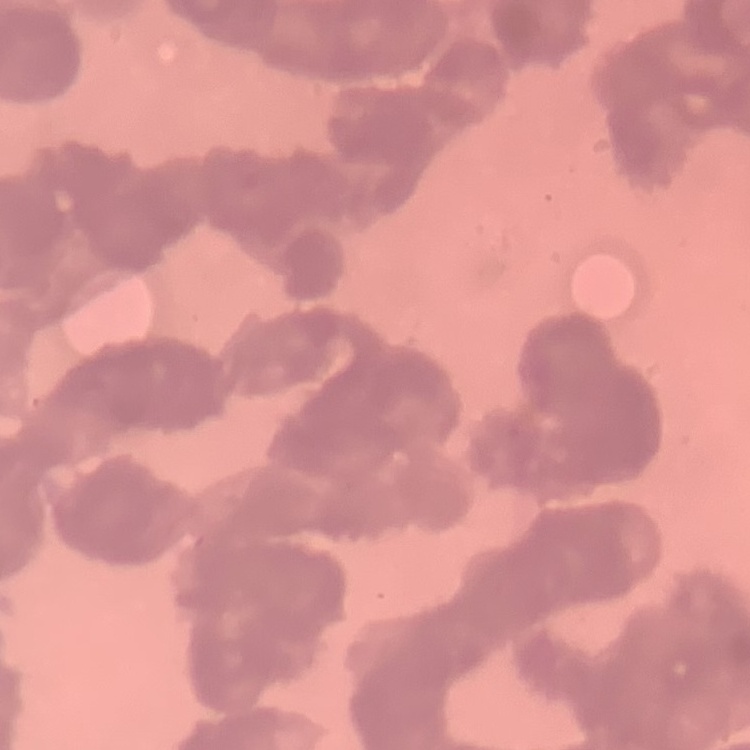

The erythrocytes show rouleaux formation. One tile cut from a larger photomicrograph. Thin peripheral smear. Field's or Giemsa stain.